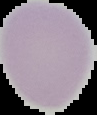

Malaria status: uninfected. Cell region segmented out of the field of view; the surrounding area is masked to black. From a thin blood film. Image is 97×115 pixels.